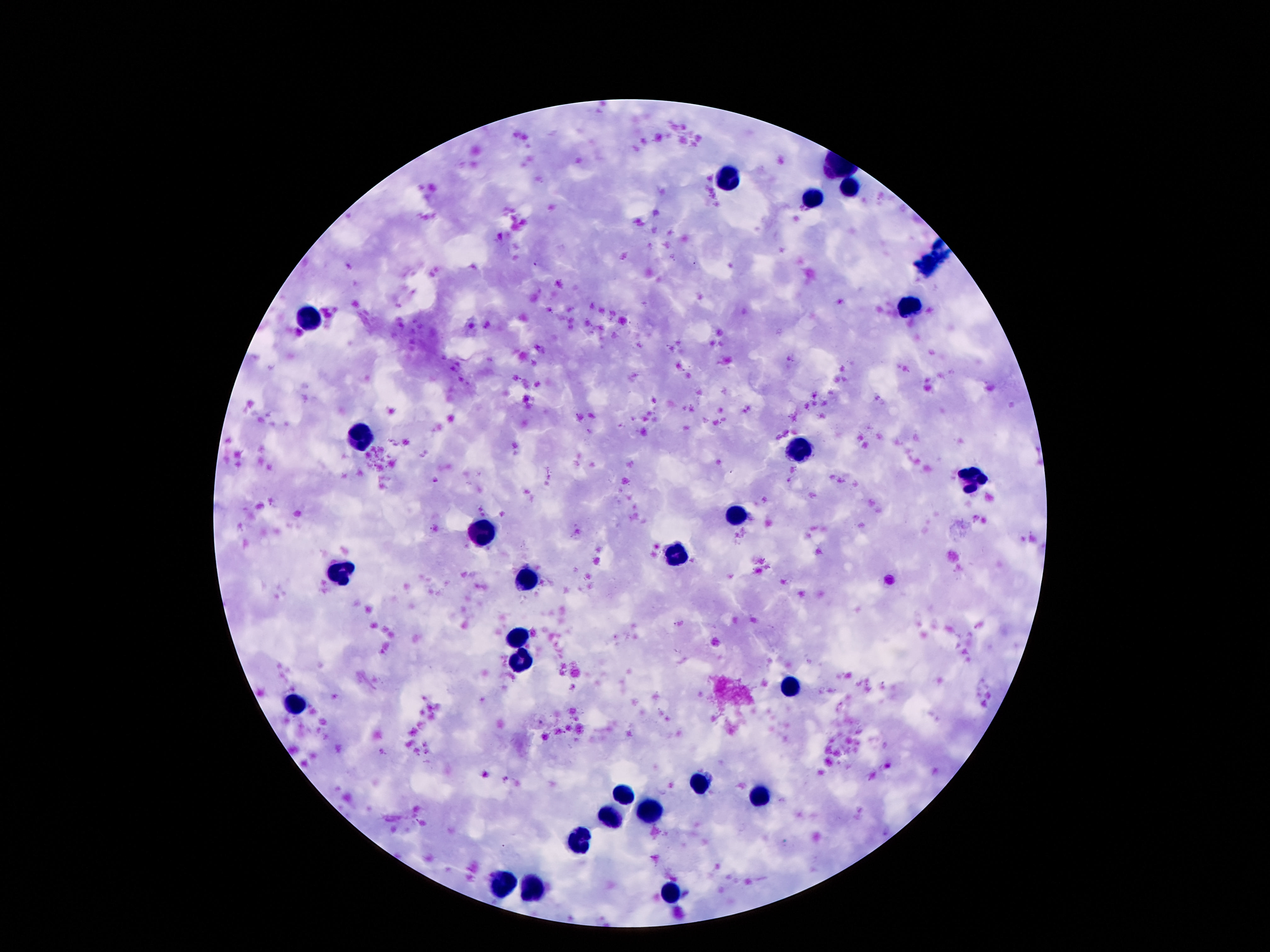

Approximate object centers, in pixels from the top-left corner.
Summary:
  - Leukocyte locations: (x=724, y=180), (x=852, y=187), (x=815, y=198), (x=912, y=310), (x=309, y=317), (x=362, y=437), (x=802, y=451), (x=976, y=476), (x=737, y=512), (x=486, y=532), (x=676, y=552), (x=340, y=573), (x=527, y=582), (x=519, y=635), (x=521, y=660), (x=793, y=685), (x=295, y=706), (x=698, y=781), (x=622, y=794), (x=762, y=796), (x=647, y=812), (x=611, y=818), (x=580, y=841), (x=505, y=885), (x=534, y=887), (x=669, y=894)
  - Preparation: thick peripheral-blood smear
  - Capture: smartphone camera through the microscope eyepiece
  - Magnification: 100x
  - Field of view: single
  - Image size: 1270×952 pixels
  - Patient malaria status: uninfected
  - Stain: Giemsa